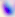

Summary:
  - Modality: photomicrograph
  - Identification: Toxoplasma gondii
  - Magnification: 400x